Locate every Plasmodium parasite.
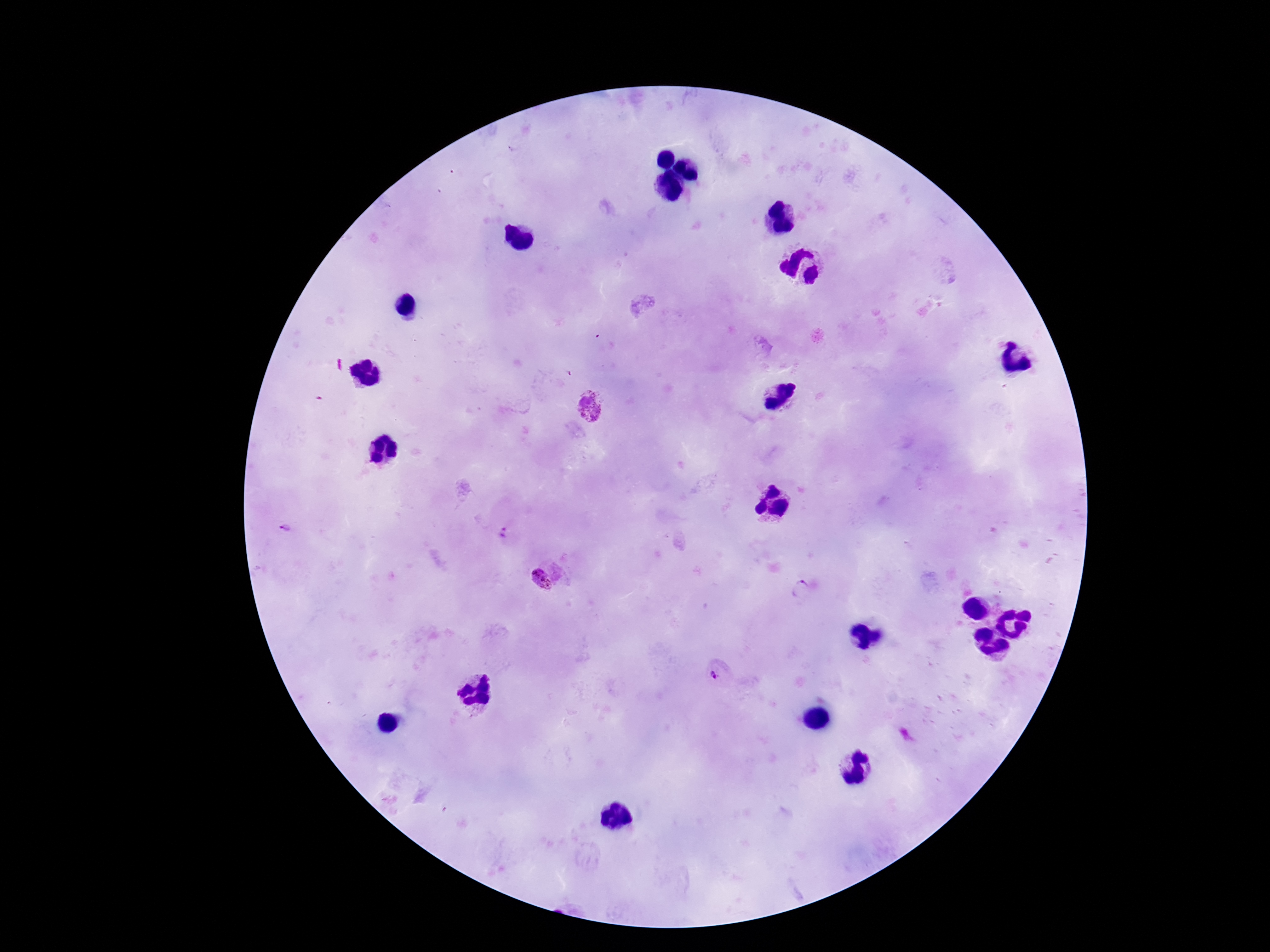

Approximate object centers, in pixels from the top-left corner.
Plasmodium parasites: (x=589, y=407), (x=285, y=529), (x=504, y=534), (x=541, y=582), (x=802, y=589), (x=714, y=676).

Summary:
  - Magnification: 100x
  - Field of view: single
  - Stain: Giemsa
  - Image size: 1270×952 pixels
  - Patient malaria status: infected
  - Preparation: thick blood film
  - Capture: smartphone camera through the microscope eyepiece